Report the malaria status of this cell.
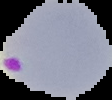
Parasitized.

The area outside the segmented cell region is set to black. Image is 112×100 pixels. From a thin blood film.